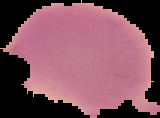

Segmented cell region on a black background. Malaria status: uninfected. From a thin blood smear. Image is 160×118 pixels.